Outline each blood parasite and name the species.
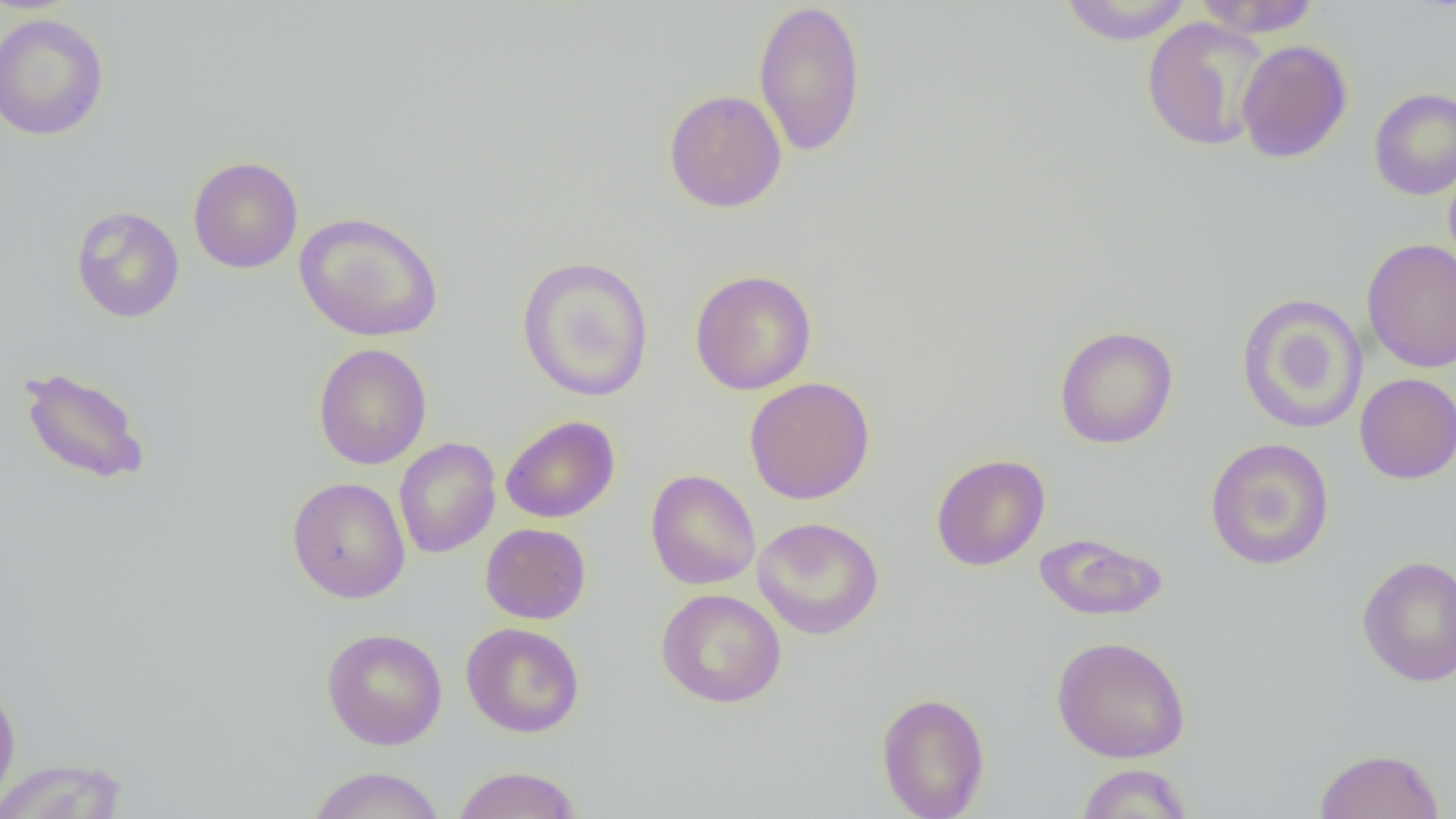
No blood parasites seen.

Summary:
  - Coordinate format: approximate bounding boxes as [x1, y1, x2, y2] in pixels
  - Uninfected red blood cell locations: [753, 0, 867, 157], [1058, 0, 1195, 46], [1192, 0, 1322, 38], [0, 12, 110, 141], [1141, 17, 1270, 151], [1236, 39, 1353, 164], [1369, 87, 1456, 200], [663, 88, 787, 213], [188, 156, 303, 273], [1443, 164, 1456, 276], [70, 205, 184, 323], [293, 211, 445, 342], [1361, 238, 1456, 373], [516, 255, 655, 403], [690, 268, 817, 395], [1236, 293, 1368, 434], [1054, 325, 1178, 449], [313, 342, 432, 470], [19, 366, 150, 485], [1354, 373, 1456, 484], [744, 376, 876, 504], [500, 415, 620, 523], [394, 437, 501, 559], [1205, 438, 1334, 571], [931, 453, 1050, 571], [645, 469, 761, 590], [287, 477, 411, 603], [753, 516, 884, 640], [481, 523, 591, 624], [1034, 533, 1167, 621], [1356, 555, 1456, 686], [656, 588, 787, 708], [461, 622, 585, 738], [321, 627, 448, 750], [1051, 636, 1191, 763], [0, 680, 21, 810], [876, 692, 990, 818], [1313, 746, 1445, 818], [0, 758, 128, 819], [1074, 763, 1194, 818], [452, 765, 583, 819], [305, 766, 446, 819]
  - Slide-level diagnosis: no evidence of blood parasites
  - Image size: 1456×819 pixels
  - Magnification: 1000x
  - Preparation: thin blood smear
  - Modality: light microscopy
  - Field of view: single